Classify this cell by malaria status.
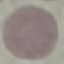

It is uninfected.

stain = Giemsa
capture = smartphone camera at the microscope eyepiece
preparation = thin blood smear
image type = cell patch, automatically extracted from a larger field of view and resized to 64 × 64 pixels